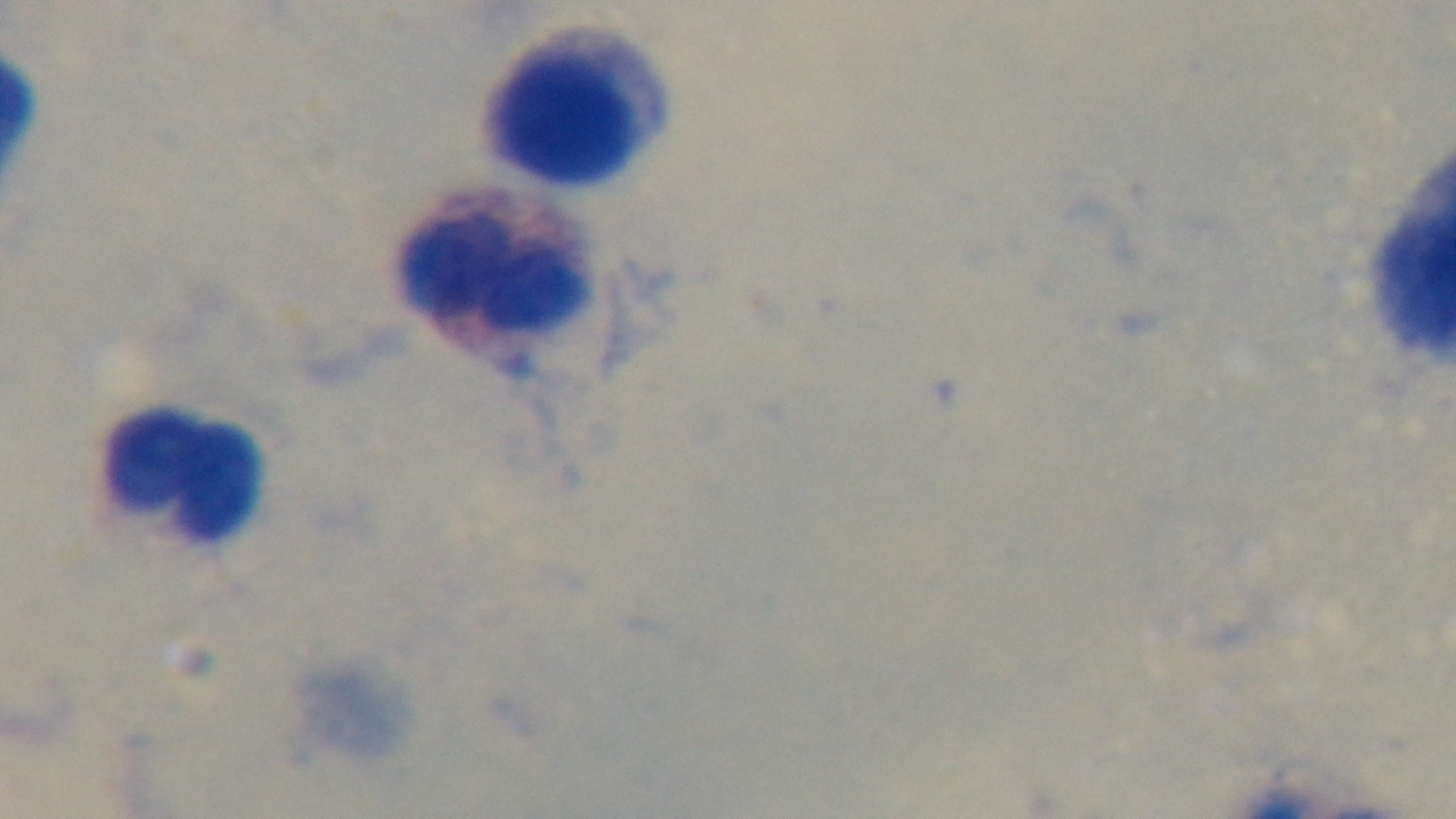
Summary:
  - Malaria status: uninfected
  - Objective: 100x oil immersion
  - Modality: light microscopy
  - Preparation: thick blood film
  - Field of view: one from the slide
  - Capture: mounted 4K digital camera
  - Stain: Giemsa